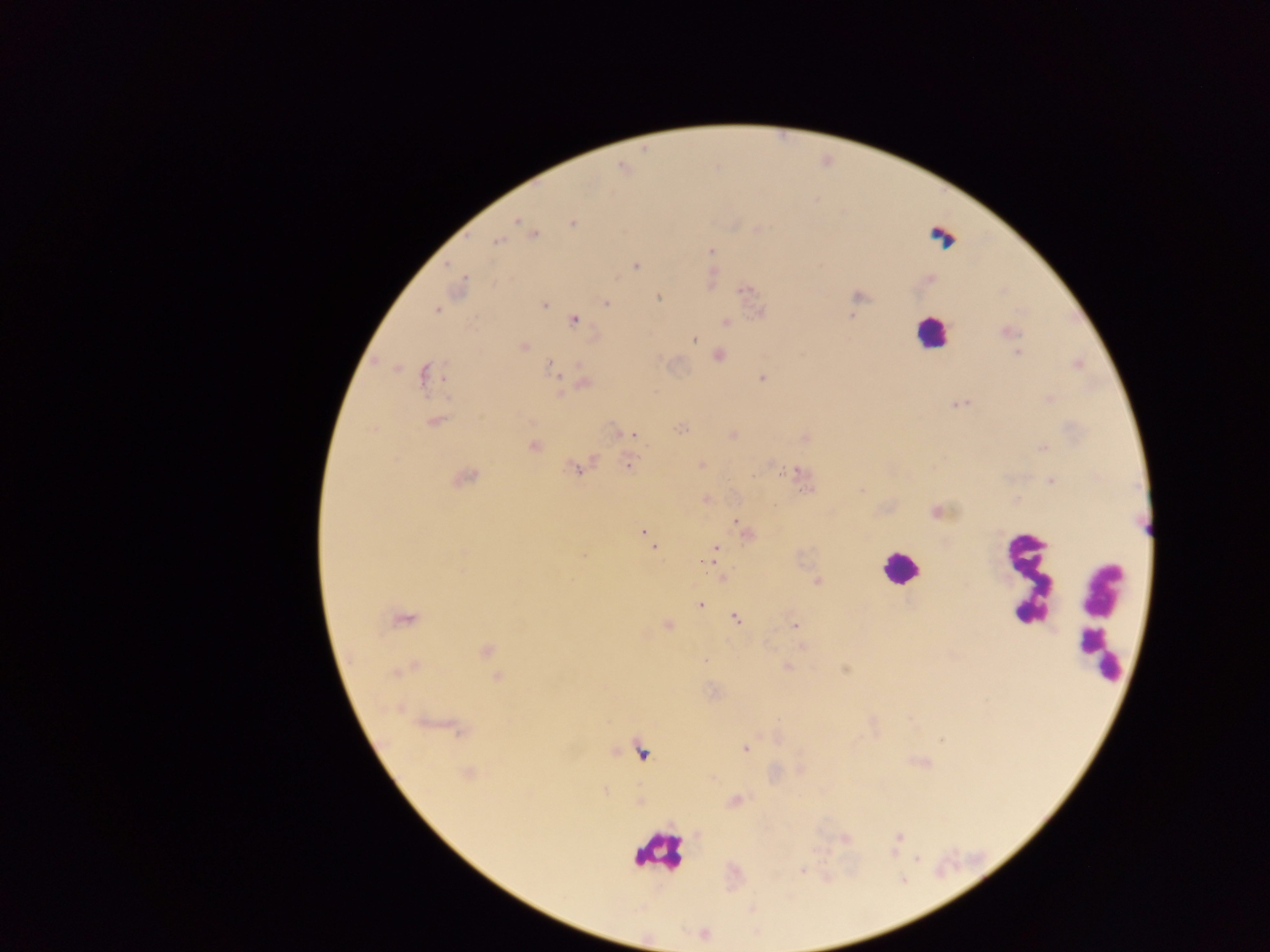

Approximate centers as [x, y] in pixels.
Summary:
  - Leukocyte locations: [932, 327], [900, 569], [1034, 584], [1099, 635], [657, 854]
  - Plasmodium parasite locations: [516, 221], [534, 233], [496, 242], [710, 250], [636, 266], [463, 279], [858, 295], [658, 296], [606, 304], [544, 306], [437, 311], [851, 314], [574, 321], [725, 321], [693, 340], [523, 346], [557, 373], [422, 375], [760, 376], [953, 405], [635, 434], [628, 461], [577, 467], [784, 470], [1052, 480], [804, 489], [734, 521], [642, 531], [654, 547], [716, 549], [709, 560], [701, 605], [736, 617], [794, 625], [705, 660], [743, 750]
  - Preparation: thick blood film
  - Field of view: single
  - Image size: 1270×952 pixels
  - Country: Ghana
  - Capture: mobile-phone photograph through a microscope